Comment on the morphology of the red blood cells.
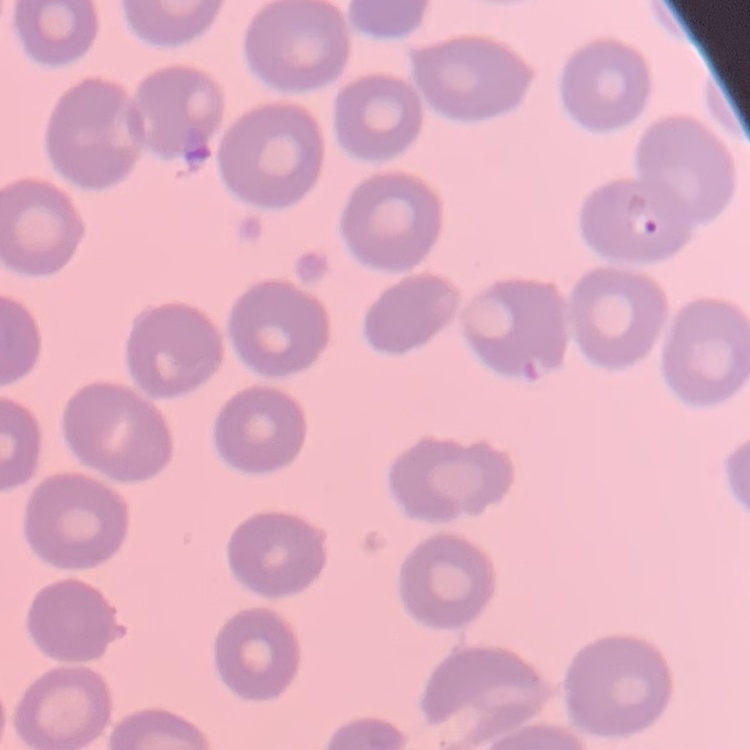

They show no rouleaux formation.

Summary:
  - Preparation: thin blood smear
  - Stain: Field's or Giemsa
  - Image type: one tile cut from a larger photomicrograph